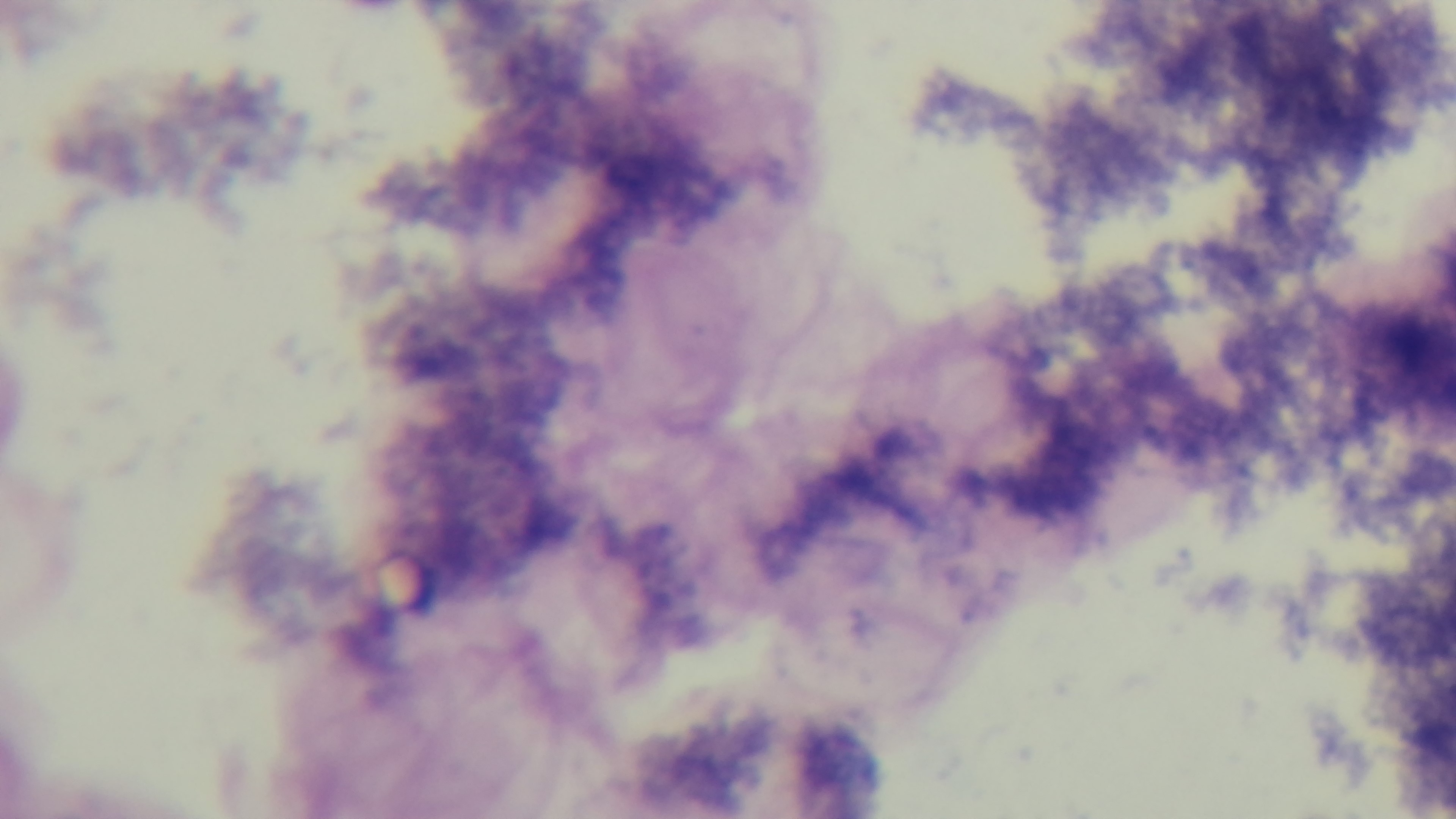

Summary:
  - Field of view: single
  - Objective: 100x oil immersion
  - Preparation: thick smear
  - Capture: mounted 4K digital camera
  - Stain: Giemsa
  - Modality: light microscopy
  - Malaria status: uninfected